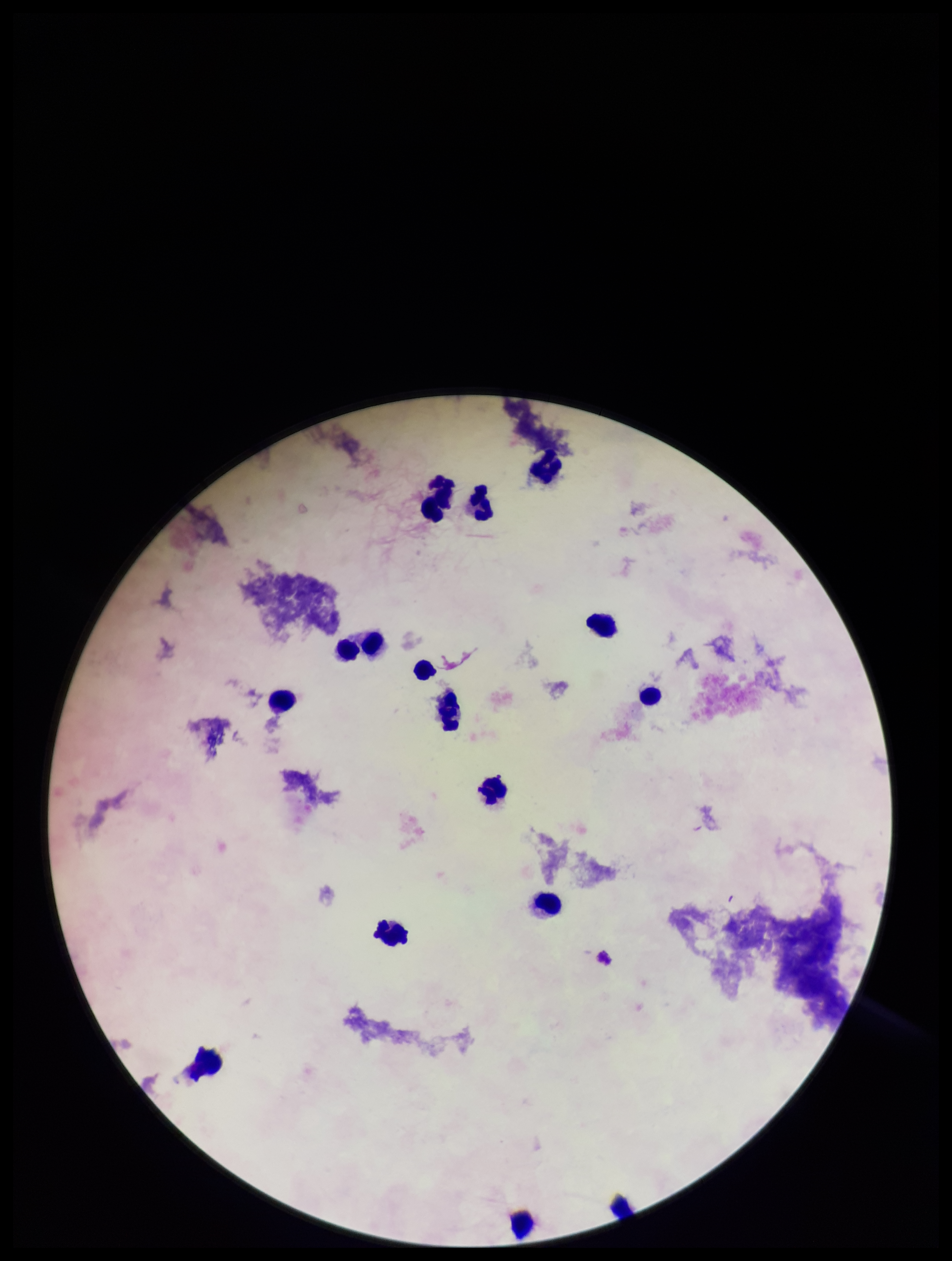
{
  "field_of_view": "one from this slide",
  "image_size": "952×1261 pixels",
  "capture": "smartphone photograph through the microscope eyepiece",
  "stain": "Giemsa",
  "patient_malaria_status": "negative",
  "parasite_count": 0,
  "leukocyte_count": 15,
  "plasmodium_parasites": "none identified",
  "preparation": "thick blood smear"
}